Describe the morphology of the red blood cells.
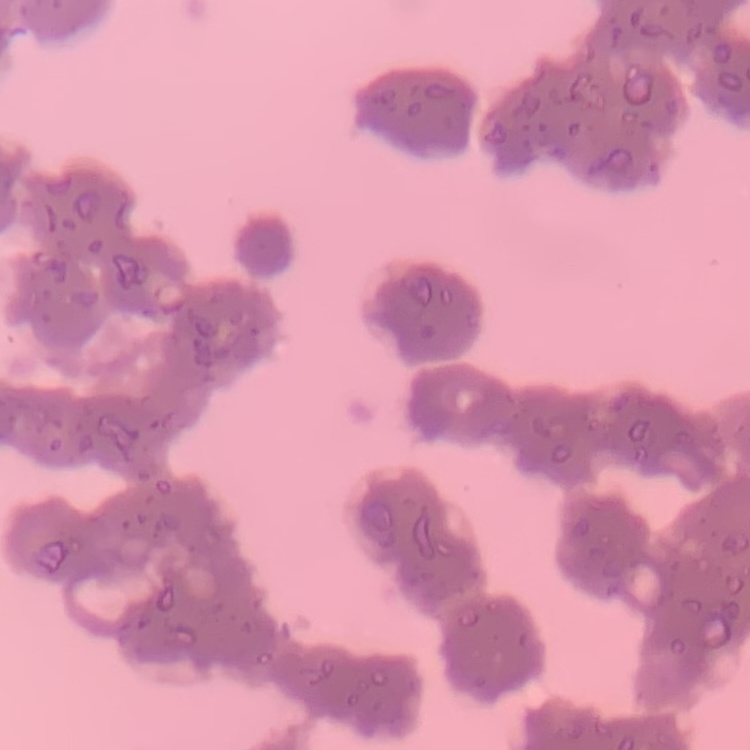

Rouleaux formation.

Summary:
  - Stain: Field's or Giemsa
  - Image type: square crop of a larger photomicrograph
  - Preparation: thin blood smear